Classify this cell by malaria status.
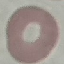

Uninfected.

Summary:
  - Image type: automatically extracted cell patch, resized to 64 × 64 pixels
  - Capture: smartphone camera at the microscope eyepiece
  - Preparation: thin blood film
  - Stain: Giemsa